Assess this cell for malaria.
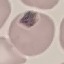
Uninfected.

preparation: thin smear
capture: smartphone through the microscope eyepiece
stain: Giemsa
image_type: cell patch, automatically extracted from a larger field of view and resized to 64 × 64 pixels